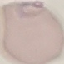
Malaria status: parasitized. Photographed with a smartphone camera at the microscope eyepiece. Thin smear of blood. Automatically extracted cell patch, resized to 64 × 64 pixels. Giemsa-stained preparation.